State which parasite is depicted.
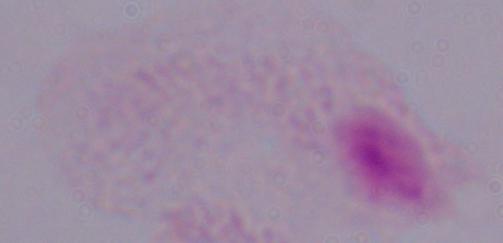
This is a trichomonad.

Captured at 1000x magnification. Photomicrograph.